Name the blood parasite species.
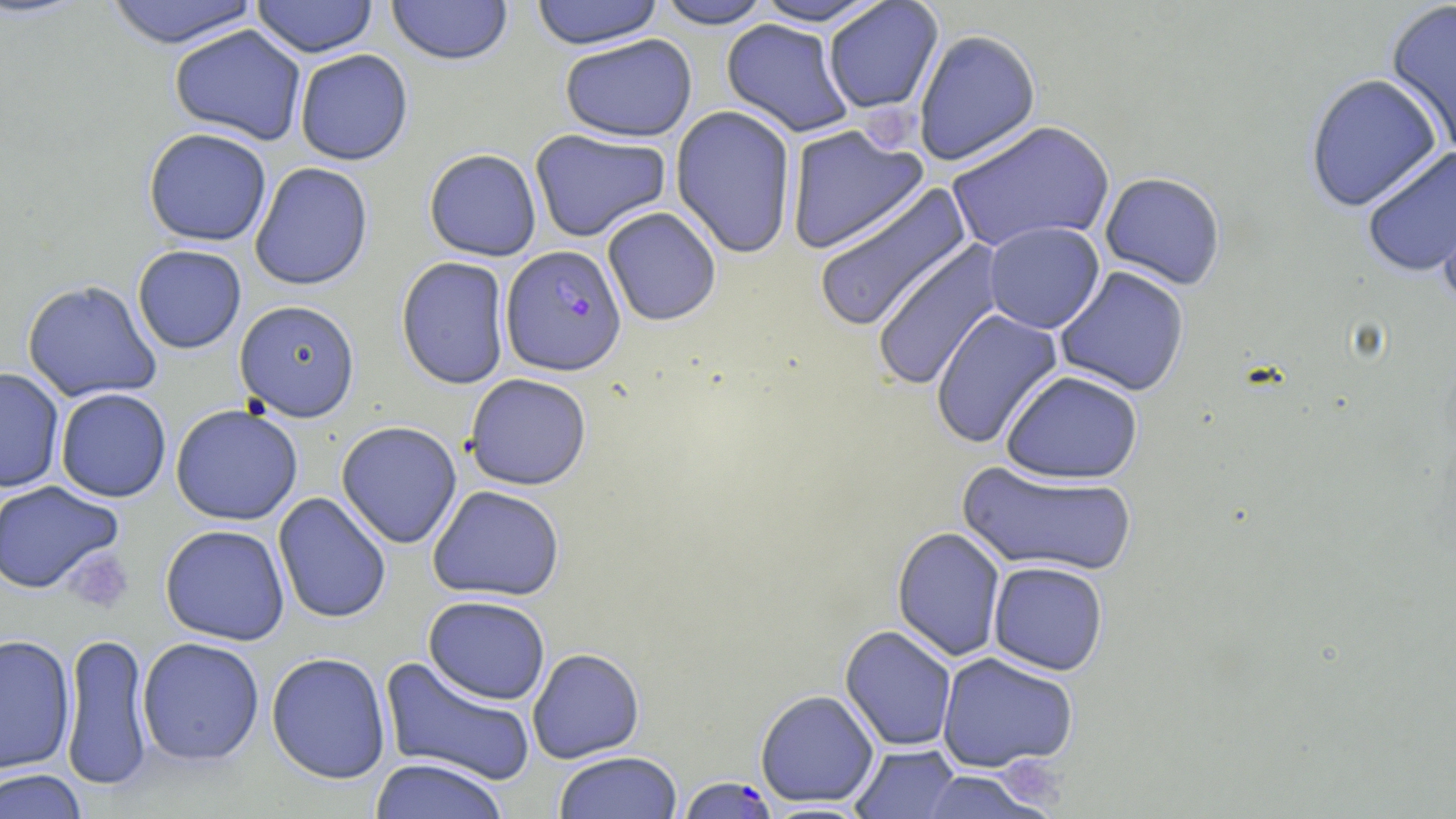
Plasmodium falciparum.

{
  "uninfected_red_blood_cell_locations": "approximate bounding boxes as (x1,y1)-(x2,y2) corner pairs in pixels: (102,0)-(261,48), (251,0)-(378,57), (386,0)-(513,66), (529,0)-(665,49), (653,0)-(777,29), (747,0)-(892,27), (1384,0)-(1456,155), (822,1)-(943,115), (721,19)-(855,138), (168,24)-(307,145), (913,29)-(1041,166), (559,33)-(697,142), (294,48)-(413,166), (1305,72)-(1443,212), (671,105)-(797,259), (945,120)-(1116,253), (784,124)-(929,255), (143,127)-(272,247), (529,128)-(671,242), (1360,145)-(1456,278), (423,148)-(542,261), (249,162)-(374,291), (1099,172)-(1227,291), (1433,178)-(1455,310), (811,181)-(973,334), (602,206)-(722,326), (983,221)-(1105,334), (870,240)-(1005,392), (132,244)-(246,354), (396,256)-(511,390), (1054,266)-(1191,397), (21,279)-(163,404), (234,300)-(361,421), (930,307)-(1064,449), (0,367)-(65,494), (1000,370)-(1144,485), (464,373)-(592,490), (55,388)-(172,502), (170,404)-(303,525), (336,420)-(462,549), (957,461)-(1139,577), (0,480)-(125,595), (427,485)-(565,601), (273,492)-(392,624), (160,524)-(290,646), (892,527)-(1006,662), (987,561)-(1109,675), (423,595)-(551,705), (840,625)-(958,751), (59,632)-(154,792), (0,634)-(76,775), (137,636)-(265,766), (527,648)-(645,763), (265,651)-(392,784), (936,651)-(1080,773), (379,656)-(537,788), (755,689)-(879,807), (850,743)-(960,818), (553,751)-(683,819), (369,757)-(510,819), (1,768)-(89,819), (915,770)-(1055,819), (758,801)-(875,818)",
  "plasmodium_falciparum_infected_red_blood_cell_locations": "approximate bounding boxes as (x1,y1)-(x2,y2) corner pairs in pixels: (500,244)-(627,375), (677,775)-(778,819)",
  "image_size": "1456×819 pixels",
  "magnification": "1000x",
  "platelet_locations": "approximate bounding boxes as (x1,y1)-(x2,y2) corner pairs in pixels: (64,547)-(134,615)",
  "stain": "May-Grünwald-Giemsa",
  "modality": "light microscopy",
  "preparation": "thin blood film",
  "field_of_view": "one of a larger specimen"
}